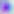

magnification = 400x
identification = Toxoplasma gondii
modality = photomicrograph